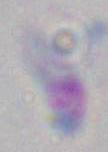

Summary:
  - Modality: micrograph
  - Magnification: 1000x
  - Identification: Toxoplasma gondii